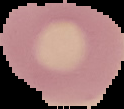

Summary:
  - Image type: segmented cell region with the area outside set to black
  - Image size: 124×109 pixels
  - Preparation: thin blood film
  - Result: no Plasmodium parasites seen